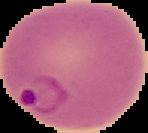

Summary:
  - Image type: cell region segmented out of the field of view; surrounding area masked to black
  - Image size: 148×133 pixels
  - Malaria status: parasitized
  - Preparation: thin blood film